Outline platelets.
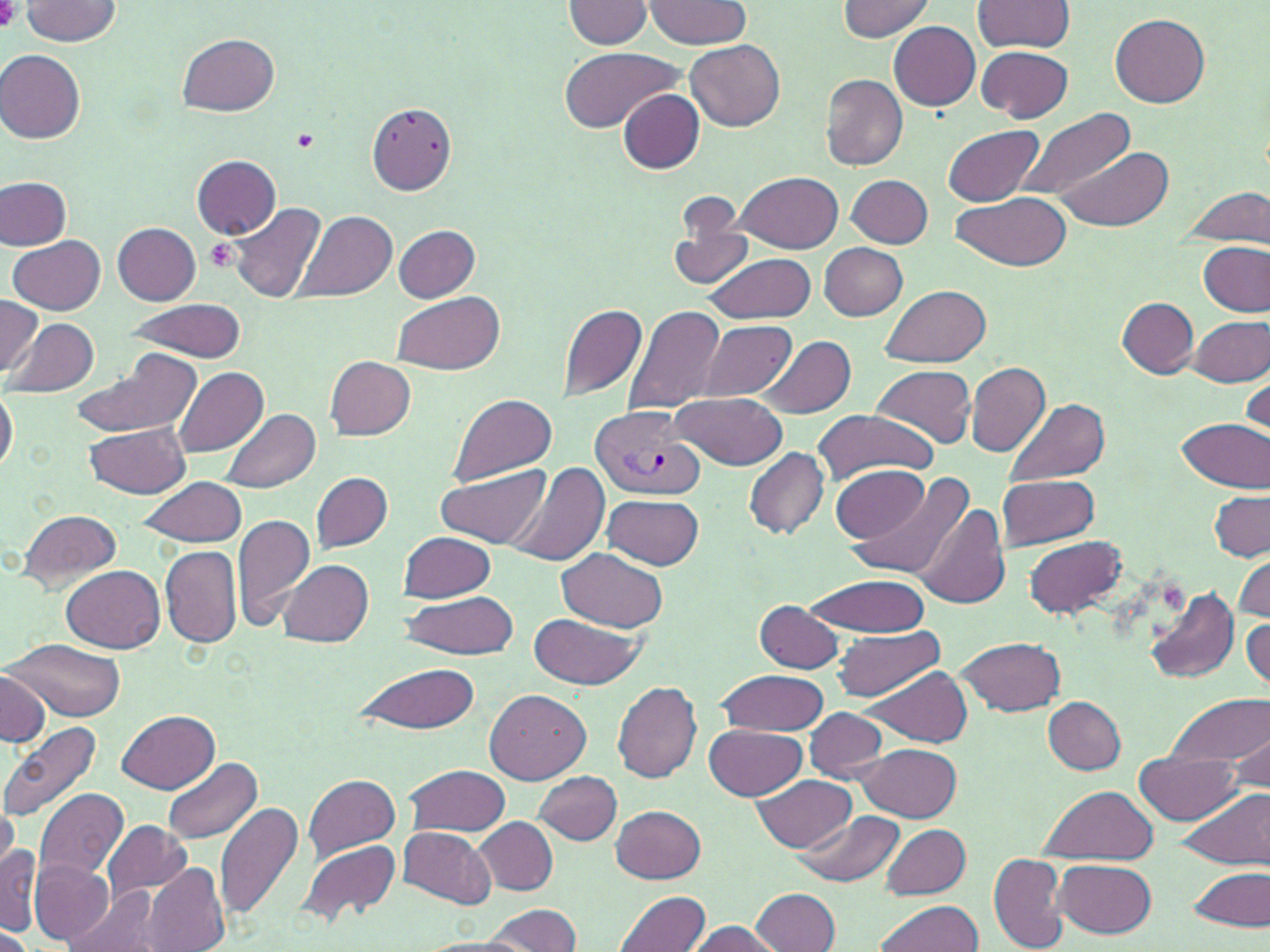
Approximate bounding boxes as (x1,y1)-(x2,y2) corner pairs in pixels.
Platelets: (0,0)-(22,31), (291,127)-(320,151), (205,239)-(240,273).

Summary:
  - Uninfected red blood cell locations: (647,0)-(750,48), (838,0)-(935,39), (972,0)-(1075,54), (564,1)-(655,49), (19,2)-(123,45), (1110,13)-(1211,107), (889,21)-(979,111), (179,33)-(280,116), (686,39)-(786,132), (976,46)-(1073,122), (557,47)-(684,131), (2,51)-(87,144), (820,74)-(908,170), (619,90)-(705,174), (367,101)-(459,194), (1012,108)-(1136,202), (943,125)-(1043,206), (1052,145)-(1174,230), (192,155)-(281,239), (733,171)-(841,253), (847,174)-(933,249), (0,176)-(72,249), (3,177)-(85,312), (1184,187)-(1268,249), (951,190)-(1072,271), (230,202)-(325,306), (295,209)-(399,303), (668,219)-(757,292), (114,222)-(202,305), (392,225)-(481,301), (10,237)-(104,314), (1199,241)-(1268,316), (819,243)-(907,321), (703,254)-(817,324), (883,285)-(991,367), (392,289)-(506,374), (0,296)-(41,379), (1117,297)-(1198,378), (124,300)-(247,361), (558,302)-(649,401), (623,304)-(727,416), (1188,315)-(1268,385), (11,316)-(100,397), (699,319)-(797,401), (756,336)-(857,420), (69,351)-(200,437), (325,356)-(415,439), (964,360)-(1050,457), (871,364)-(977,450), (172,365)-(270,458), (1242,373)-(1270,446), (0,386)-(17,477), (450,392)-(557,485), (670,392)-(789,469), (1004,398)-(1111,487), (221,408)-(321,493), (814,410)-(937,485), (1176,417)-(1267,493), (81,422)-(192,498), (742,446)-(830,540), (507,462)-(610,567), (833,465)-(929,542), (438,466)-(547,549), (312,471)-(393,553), (848,471)-(978,581), (997,475)-(1099,549), (138,476)-(247,548), (1209,491)-(1269,561), (602,493)-(704,569), (915,504)-(1009,611), (18,509)-(123,592), (233,512)-(316,629), (399,531)-(495,601), (1024,535)-(1127,619), (161,544)-(241,648), (558,548)-(670,634), (1234,556)-(1270,624), (280,560)-(373,646), (62,565)-(164,653), (801,572)-(933,637), (1147,588)-(1239,684), (401,591)-(520,659), (755,600)-(844,673), (530,613)-(643,690), (1242,619)-(1269,692), (834,626)-(943,700), (957,637)-(1065,715), (8,639)-(127,721), (354,662)-(482,735), (860,664)-(974,748), (0,669)-(50,748), (715,670)-(829,736), (612,680)-(701,785), (485,688)-(589,784), (1167,695)-(1269,768), (1043,696)-(1126,774), (804,708)-(887,782), (117,710)-(218,793), (1,721)-(104,822), (702,725)-(807,799), (1230,731)-(1267,790), (859,743)-(961,821), (1136,752)-(1242,825), (163,756)-(262,845), (404,764)-(510,836), (533,769)-(622,845), (303,773)-(399,859), (749,775)-(859,853), (1036,783)-(1159,863), (1175,786)-(1270,872), (34,788)-(128,883), (0,799)-(17,876), (216,802)-(305,925), (612,805)-(707,883), (793,810)-(905,889), (475,816)-(558,894), (103,821)-(193,901), (880,823)-(970,899), (398,826)-(496,909), (297,839)-(399,924), (1,847)-(38,935), (987,853)-(1069,952), (29,859)-(113,944), (1054,859)-(1157,938), (142,863)-(230,952), (1189,864)-(1268,934), (69,884)-(162,952), (749,887)-(841,952), (614,890)-(710,952), (873,899)-(983,952), (487,903)-(580,952), (685,919)-(782,952), (0,927)-(36,951), (413,937)-(532,952)
  - Plasmodium vivax-infected red blood cell locations: (588,406)-(704,502)
  - Slide-level diagnosis: Plasmodium vivax
  - Modality: light microscopy
  - Image size: 1270×952 pixels
  - Magnification: 1000x
  - Stain: May-Grünwald-Giemsa
  - Field of view: one of a larger specimen
  - Preparation: thin blood smear